State the blood parasite species.
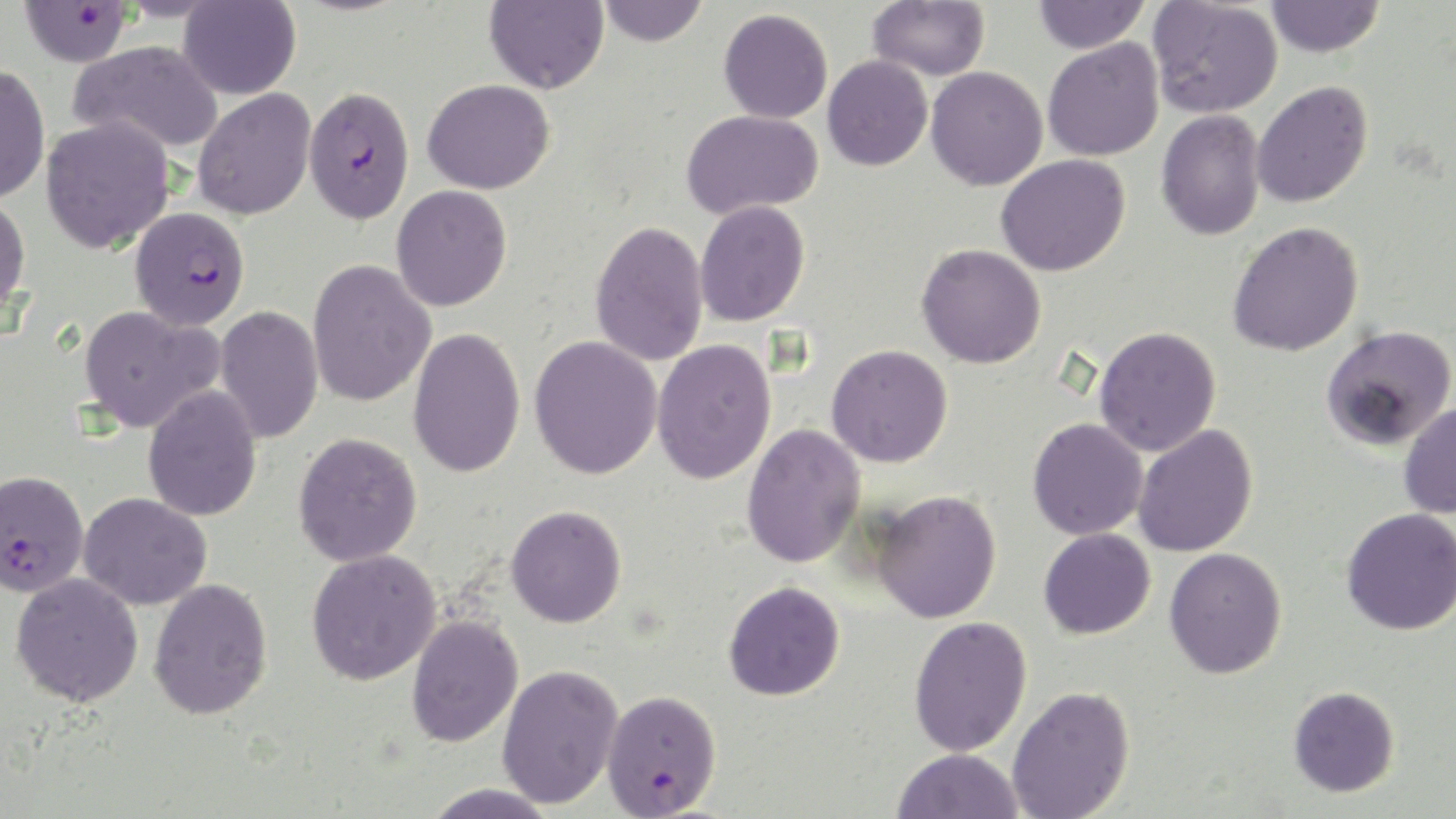

Plasmodium falciparum.

Approximate bounding boxes as (x1,y1)-(x2,y2) corner pairs in pixels. Uninfected red blood cell locations: (484,0)-(609,94), (597,0)-(710,46), (867,0)-(990,81), (1032,0)-(1150,54), (1148,0)-(1283,119), (1264,0)-(1385,58), (178,1)-(301,100), (718,8)-(833,123), (1042,38)-(1165,162), (69,40)-(223,155), (823,55)-(933,171), (0,63)-(50,204), (926,67)-(1048,190), (422,78)-(556,194), (1252,80)-(1373,208), (192,88)-(316,220), (681,109)-(824,219), (1156,110)-(1266,241), (40,116)-(176,255), (996,154)-(1130,276), (391,185)-(512,312), (0,194)-(31,318), (695,200)-(810,326), (589,221)-(709,367), (1227,221)-(1364,357), (916,243)-(1046,369), (306,260)-(435,407), (78,305)-(222,433), (215,305)-(324,444), (1321,325)-(1456,449), (1094,326)-(1222,457), (407,327)-(526,478), (529,335)-(663,480), (651,339)-(777,485), (826,344)-(953,468), (143,385)-(263,522), (1398,401)-(1456,519), (1027,418)-(1148,540), (741,422)-(866,569), (1133,424)-(1259,557), (293,432)-(423,567), (871,488)-(1002,624), (79,492)-(212,610), (506,505)-(627,628), (1341,507)-(1456,635), (1038,528)-(1156,640), (1164,547)-(1288,679), (306,548)-(441,685), (10,572)-(144,707), (148,577)-(273,720), (724,580)-(845,701), (406,614)-(524,748), (909,615)-(1033,757), (496,663)-(622,809), (1007,685)-(1135,819), (1288,685)-(1400,797), (891,748)-(1024,819), (421,782)-(561,819). Plasmodium falciparum-infected red blood cell locations: (18,1)-(132,67), (303,84)-(415,225), (130,207)-(250,330), (0,469)-(89,598), (601,688)-(722,817). Captured at 1000x magnification. Image is 1456×819 pixels. Thin blood film. Light microscopy. Single field of view. May-Grünwald-Giemsa-stained preparation.